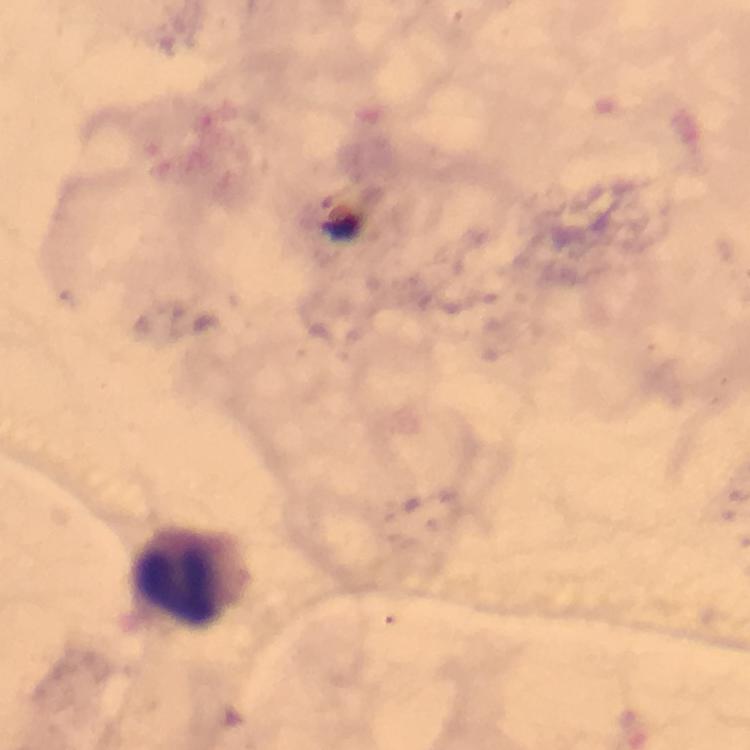 Approximate centers as {x, y} in pixels. Leukocyte locations: {191, 575}. Giemsa stain. A crop from one field of view. Image is 750×750 pixels. Immersion oil applied. Thick blood smear. Plasmodium parasites: none detected. From a diagnostic examination for malaria. 100x magnification. Photographed through the microscope with a smartphone camera.